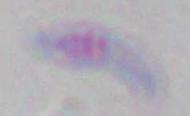
Summary:
  - Identification: Toxoplasma gondii
  - Magnification: 1000x
  - Modality: micrograph